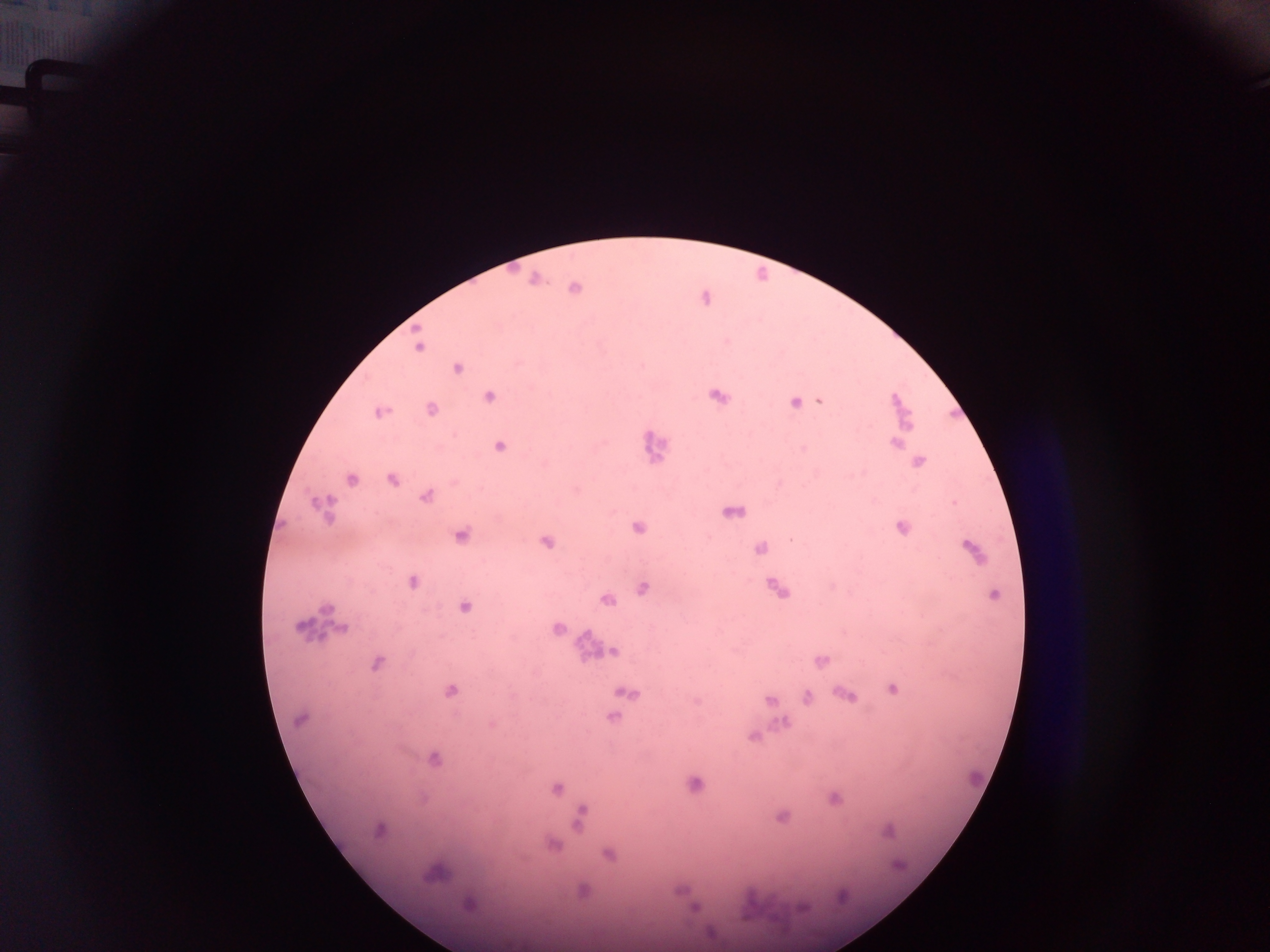 Approximate centers as (x, y) in pixels. Malaria parasite locations: (533, 280), (574, 289), (418, 346), (642, 363), (456, 368), (717, 395), (487, 396), (895, 399), (819, 401), (794, 402), (432, 408), (377, 413), (907, 425), (894, 442), (498, 447), (917, 462), (544, 463), (861, 472), (351, 480), (391, 481), (424, 497), (314, 504), (954, 504), (743, 510), (729, 513), (637, 528), (901, 528), (460, 534), (789, 539), (545, 542), (967, 546), (759, 549), (412, 582), (642, 586), (776, 589), (993, 594), (607, 599), (463, 607), (300, 627), (342, 628), (557, 629), (612, 650), (820, 661), (375, 665), (893, 688), (450, 690), (620, 692), (842, 693), (850, 695), (806, 696), (768, 700), (695, 703), (612, 717), (299, 719), (783, 722), (492, 725), (753, 737), (434, 759), (693, 783), (557, 789), (833, 800), (580, 817), (782, 817), (577, 826), (378, 830), (889, 832), (554, 848), (608, 855), (427, 876), (468, 903), (800, 907), (693, 908), (742, 918). Thick blood film. One field of view. Sample from Ghana. Image is 1270×952 pixels. Mobile-phone photograph taken through the microscope.